Assess this cell for malaria.
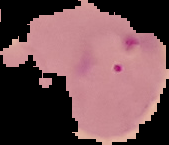
It is uninfected.

image_size: 169×145 pixels
image_type: segmented cell region with the area outside set to black
preparation: thin blood film